Locate every Plasmodium parasite.
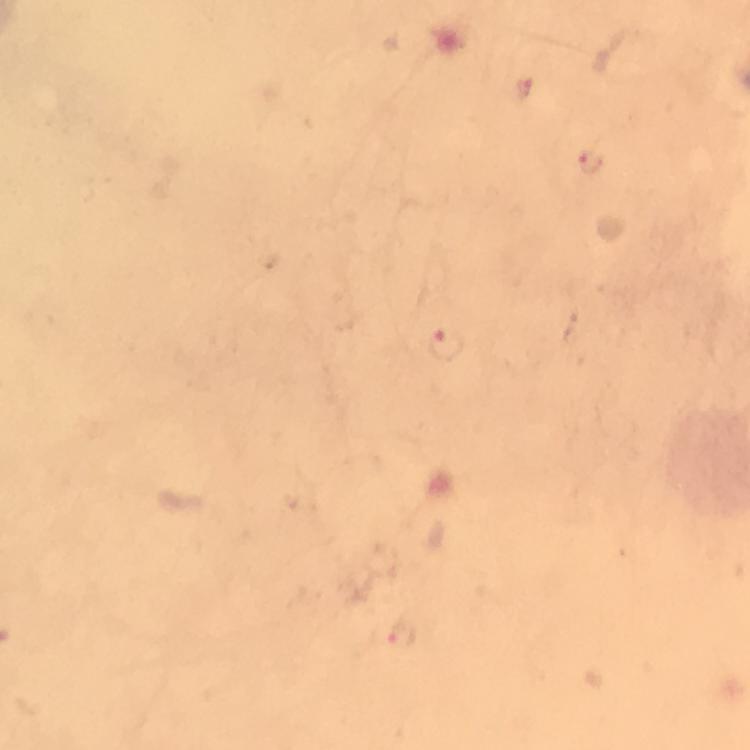

Approximate centers as {x, y} in pixels.
Plasmodium parasites: {591, 161}, {446, 344}.

Summary:
  - Magnification: 100x
  - Image size: 750×750 pixels
  - Stain: Giemsa
  - Context: from a malaria diagnostic workup
  - Immersion oil: used
  - Cropped from: a single field of view
  - Preparation: thick blood film
  - Capture: smartphone photograph through a microscope